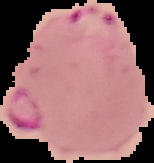

Image is 154×163 pixels. From a thin blood film. Result: malaria parasites detected. Cell region segmented out of the field of view; the surrounding area is masked to black.